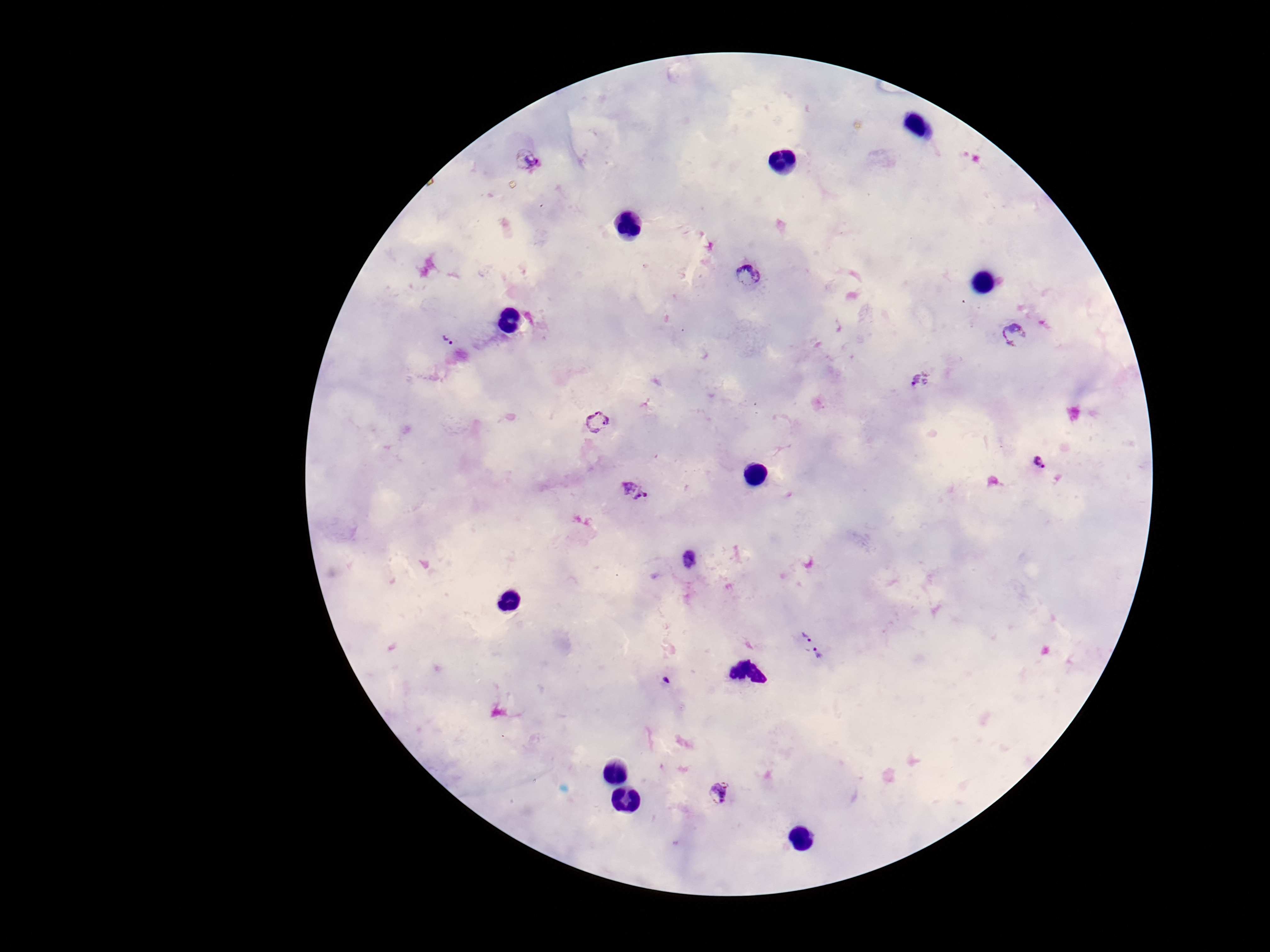

{
  "preparation": "thick blood film",
  "image_size": "1270×952 pixels",
  "magnification": "100x",
  "capture": "smartphone camera through the microscope eyepiece",
  "stain": "Giemsa",
  "patient_malaria_status": "infected",
  "field_of_view": "one from this slide",
  "plasmodium_parasite_locations": "approximate centers as [x, y] in pixels: [528, 161], [747, 275], [1015, 335], [448, 340], [921, 379], [600, 422], [1040, 463], [636, 494], [689, 561], [804, 637], [819, 659], [666, 681], [719, 793]"
}